Report the malaria status of this cell.
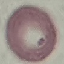
It is uninfected.

Summary:
  - Preparation: thin blood film
  - Stain: Giemsa
  - Image type: automatically extracted cell patch, resized to 64 × 64 pixels
  - Capture: smartphone through the microscope eyepiece